Assess the morphology of the erythrocytes.
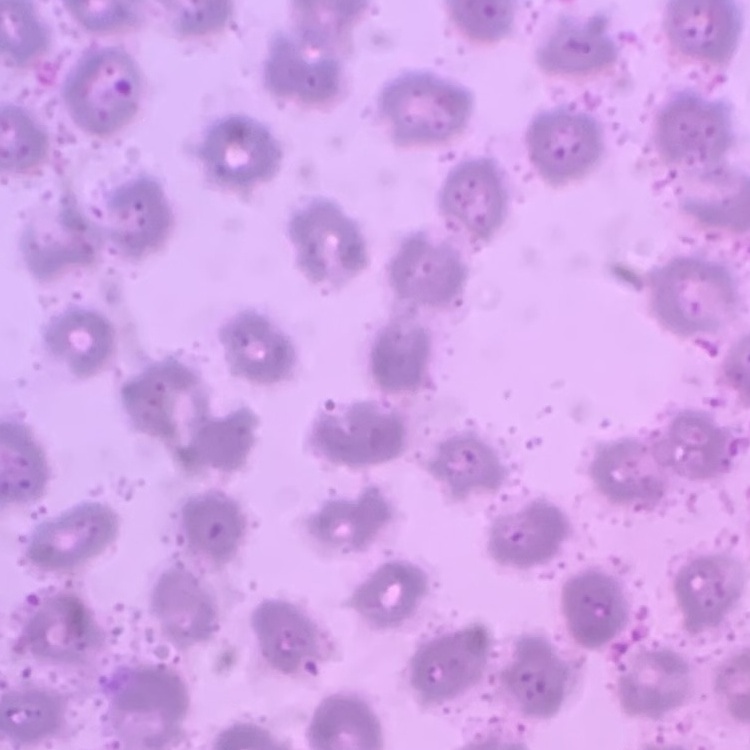

They show no rouleaux formation.

stain = Field's or Giemsa
image type = one tile cut from a larger photomicrograph
preparation = thin blood smear